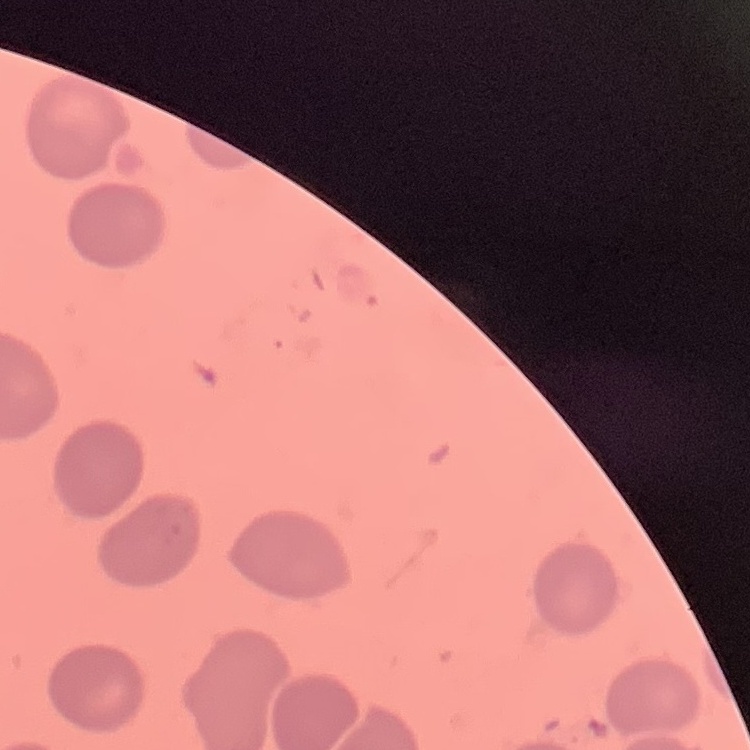

Summary:
  - Erythrocyte morphology: no rouleaux formation
  - Preparation: thin blood smear
  - Stain: Field's or Giemsa
  - Image type: square crop of a larger photomicrograph